Identify the parasite.
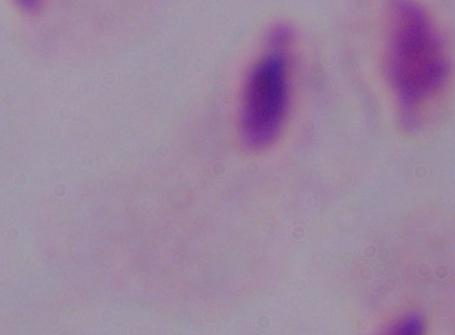
This is a trichomonad.

Summary:
  - Magnification: 1000x
  - Modality: micrograph